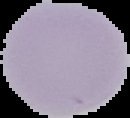 Cell region segmented out of the field of view; the surrounding area is masked to black. Image is 130×118 pixels. From a thin blood film. Malaria status: uninfected.